Locate every Babesia divergens-infected red blood cell.
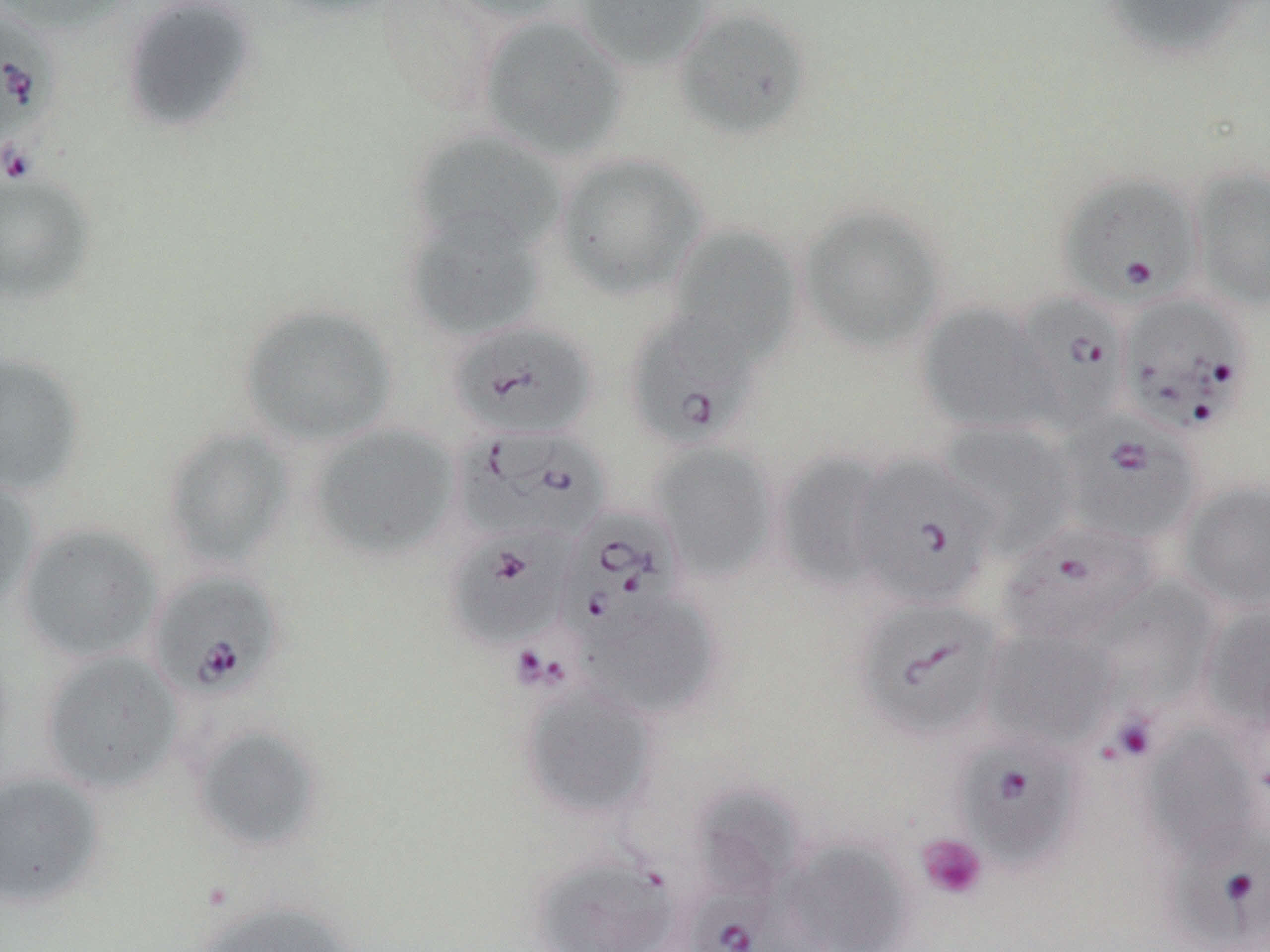
Approximate bounding boxes as (x1,y1)-(x2,y2) corner pairs in pixels.
Babesia divergens-infected red blood cells: (0,7)-(57,151), (1058,173)-(1201,306), (1011,292)-(1129,433), (1116,294)-(1253,437), (626,311)-(760,450), (448,320)-(598,440), (1060,414)-(1202,546), (452,427)-(611,545), (850,453)-(997,609), (555,506)-(686,646), (996,520)-(1158,648), (447,527)-(576,650), (146,570)-(283,700), (852,596)-(1006,744), (955,735)-(1082,873), (1166,821)-(1270,950), (686,885)-(814,952).

Uninfected red blood cell locations: (0,0)-(134,34), (120,0)-(258,135), (257,0)-(404,21), (442,0)-(577,24), (574,0)-(714,71), (1103,0)-(1253,58), (672,5)-(812,141), (477,14)-(628,161), (409,129)-(567,253), (554,152)-(708,299), (1189,167)-(1270,310), (0,172)-(95,306), (798,203)-(947,354), (404,209)-(545,342), (666,224)-(800,363), (916,302)-(1058,435), (240,303)-(398,447), (0,352)-(86,496), (938,421)-(1078,555), (308,424)-(459,560), (161,428)-(295,569), (650,442)-(779,581), (773,450)-(892,592), (0,475)-(41,612), (1178,479)-(1270,613), (16,523)-(162,662), (1091,578)-(1218,720), (575,597)-(721,719), (1198,601)-(1270,733), (981,627)-(1119,752), (41,651)-(182,793), (519,682)-(659,820), (191,725)-(321,852), (1140,725)-(1262,862), (0,770)-(106,911), (693,787)-(803,897), (782,840)-(911,952), (535,855)-(673,952), (199,901)-(352,952). Platelet locations: (916,834)-(989,901). Slide-level diagnosis: Babesia divergens. 1000x magnification. May-Grünwald-Giemsa stain. Thin blood film. Image is 1270×952 pixels. Optical microscopy. One field of a larger specimen.